Assess this cell for malaria.
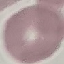
Uninfected.

Summary:
  - Preparation: thin blood film
  - Image type: automatically extracted cell patch, resized to 64 × 64 pixels
  - Capture: smartphone through the microscope eyepiece
  - Stain: Giemsa